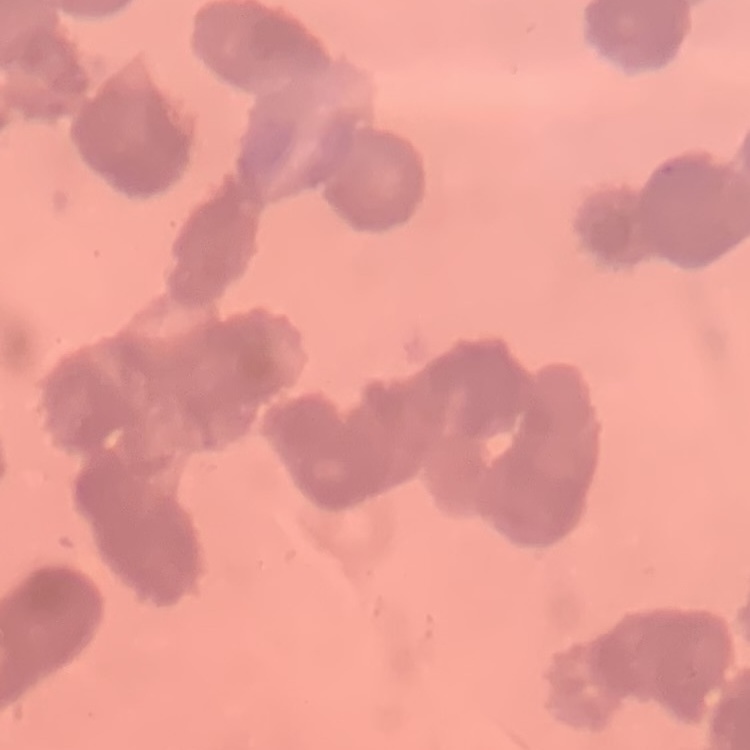

The erythrocytes exhibit rouleaux formation. Thin blood film. One tile cut from a larger photomicrograph. Field's or Giemsa stain.